Give a bounding box for every parasitised red blood cell, every trophozoite, every gametocyte, every leukocyte, and every artifact (platelet-like body, stain precipitate, or debris).
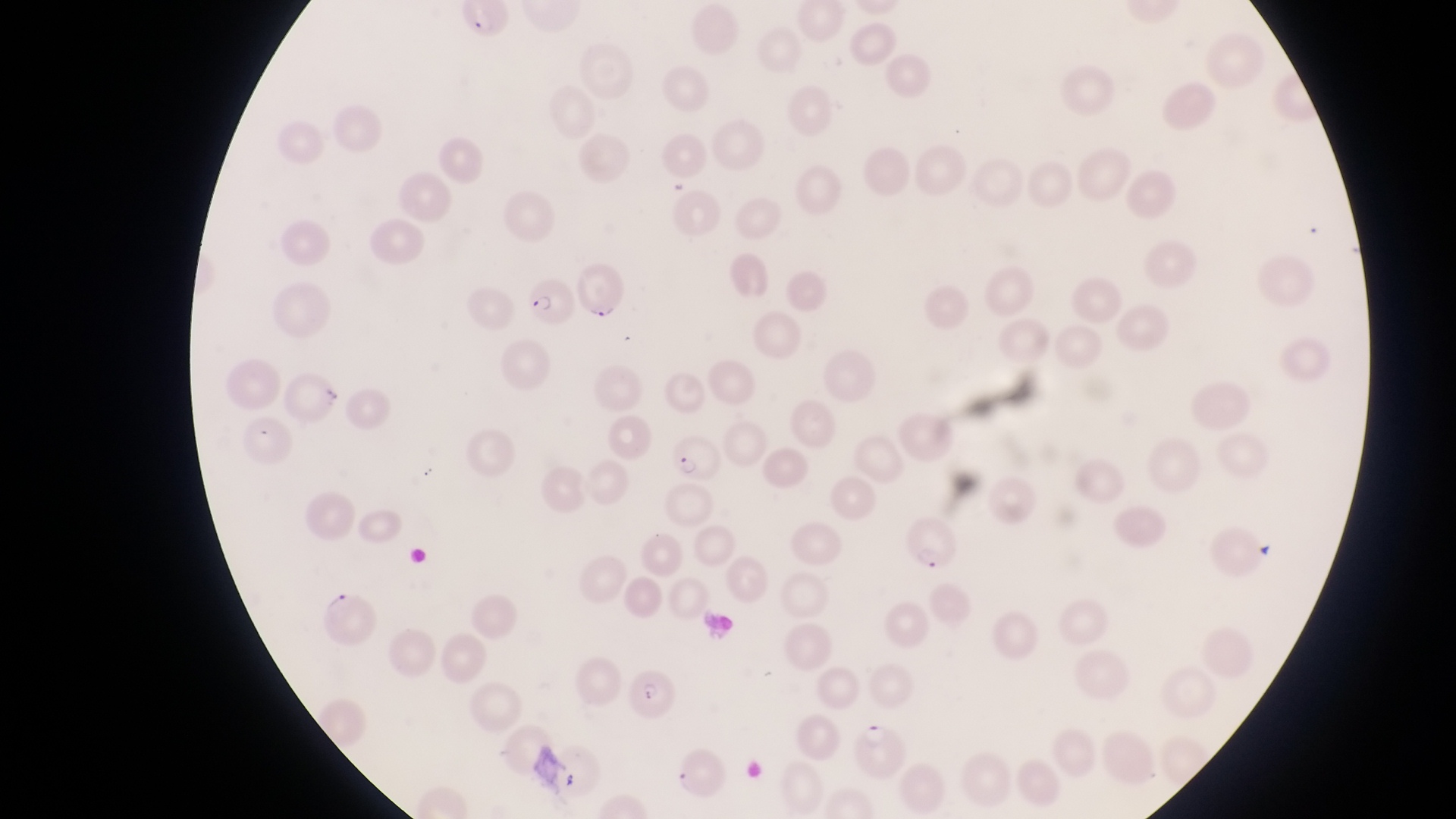
Approximate bounding boxes as (left, top, right, bottom) in pixels.
Parasitised red blood cells: (576, 259, 631, 322), (521, 278, 574, 328), (674, 436, 726, 483), (904, 513, 963, 572), (320, 588, 380, 649), (626, 674, 685, 723), (851, 720, 909, 780).
No leukocytes observed.

Summary:
  - Country: Uganda
  - Capture: smartphone photograph through the eyepiece of an Olympus CX-23 microscope
  - Image size: 1456×819 pixels
  - Magnification: 1000x
  - Preparation: thin blood film
  - Field of view: single